Locate every Babesia divergens-infected red blood cell.
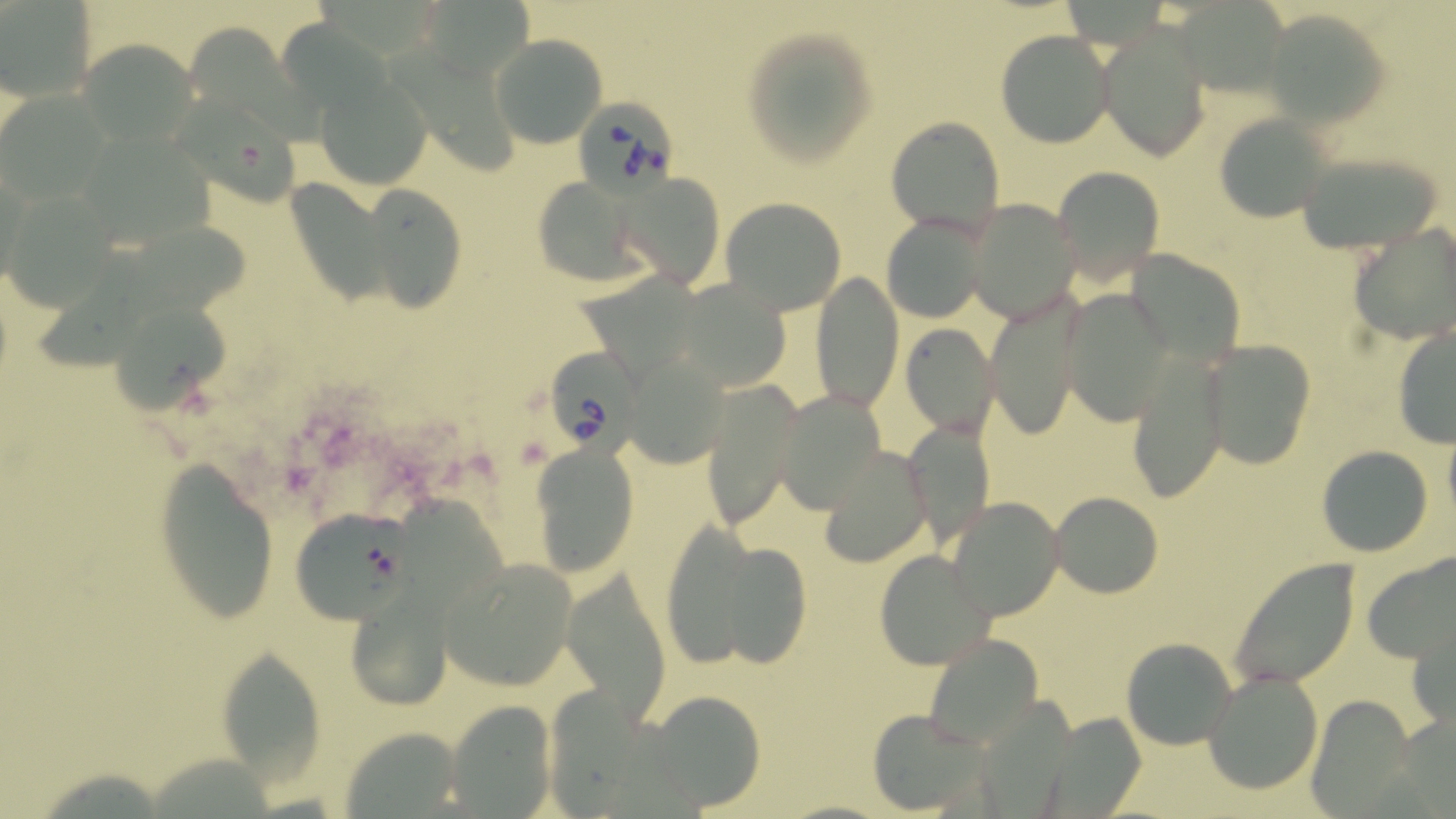
Approximate bounding boxes as [x1, y1, x2, y2] in pixels.
Babesia divergens-infected red blood cells: [578, 100, 675, 189], [546, 343, 657, 459].

Uninfected red blood cell locations: [1, 3, 95, 102], [1261, 7, 1391, 129], [739, 24, 881, 169], [1097, 27, 1211, 161], [995, 30, 1116, 148], [491, 34, 607, 148], [79, 40, 194, 146], [317, 78, 430, 188], [0, 88, 114, 202], [172, 88, 302, 203], [1214, 111, 1335, 221], [886, 118, 1005, 236], [78, 129, 213, 250], [1297, 145, 1447, 256], [1053, 167, 1166, 281], [616, 173, 726, 288], [291, 174, 390, 305], [530, 177, 649, 288], [1, 182, 120, 307], [358, 186, 467, 313], [721, 197, 846, 314], [964, 198, 1083, 322], [881, 212, 991, 323], [1349, 224, 1456, 343], [1132, 236, 1244, 367], [811, 273, 901, 412], [674, 277, 792, 390], [1064, 288, 1178, 425], [111, 294, 229, 413], [986, 296, 1088, 440], [902, 324, 999, 436], [1392, 325, 1455, 449], [1200, 339, 1318, 469], [1124, 353, 1231, 500], [622, 354, 733, 468], [699, 379, 803, 529], [774, 389, 887, 513], [903, 421, 993, 546], [1442, 429, 1456, 530], [530, 443, 640, 575], [1316, 444, 1435, 556], [820, 445, 934, 567], [153, 458, 283, 623], [1049, 491, 1162, 597], [946, 497, 1064, 622], [290, 511, 407, 624], [684, 532, 816, 668], [874, 549, 996, 671], [1361, 550, 1456, 666], [436, 556, 579, 691], [1229, 557, 1360, 691], [560, 570, 672, 718], [339, 584, 461, 710], [1410, 625, 1455, 726], [921, 632, 1045, 750], [1122, 637, 1236, 748], [214, 643, 330, 779], [1156, 648, 1300, 771], [1204, 668, 1324, 795], [645, 692, 766, 812], [1305, 694, 1414, 813], [446, 699, 558, 816], [867, 709, 994, 813], [335, 725, 467, 812]. Slide-level diagnosis: Babesia divergens. One field of a larger specimen. Captured at 1000x magnification. Image is 1456×819 pixels. Thin blood smear. Light microscopy. May-Grünwald-Giemsa stain.